Assess this cell for malaria.
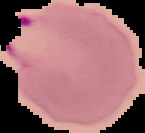

It is parasitized.

Summary:
  - Image type: cell region segmented out of the field of view; surrounding area masked to black
  - Preparation: thin blood film
  - Image size: 145×133 pixels